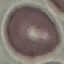
Summary:
  - Malaria status: uninfected
  - Preparation: thin smear
  - Stain: Giemsa
  - Capture: smartphone camera at the microscope eyepiece
  - Image type: cell patch, automatically extracted from a larger field of view and resized to 64 × 64 pixels